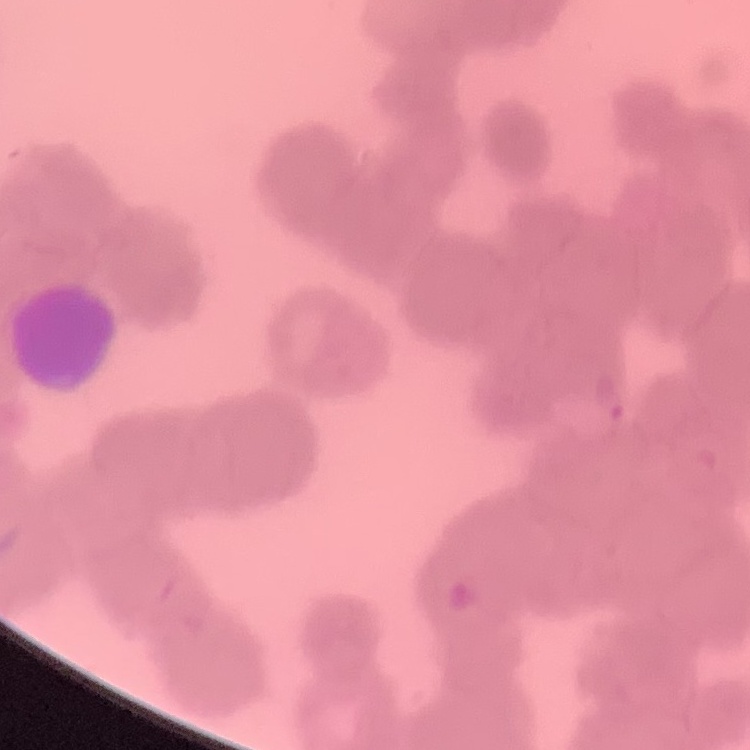

erythrocyte morphology = rouleaux formation
image type = one tile cut from a larger photomicrograph
stain = Field's or Giemsa
preparation = thin peripheral smear